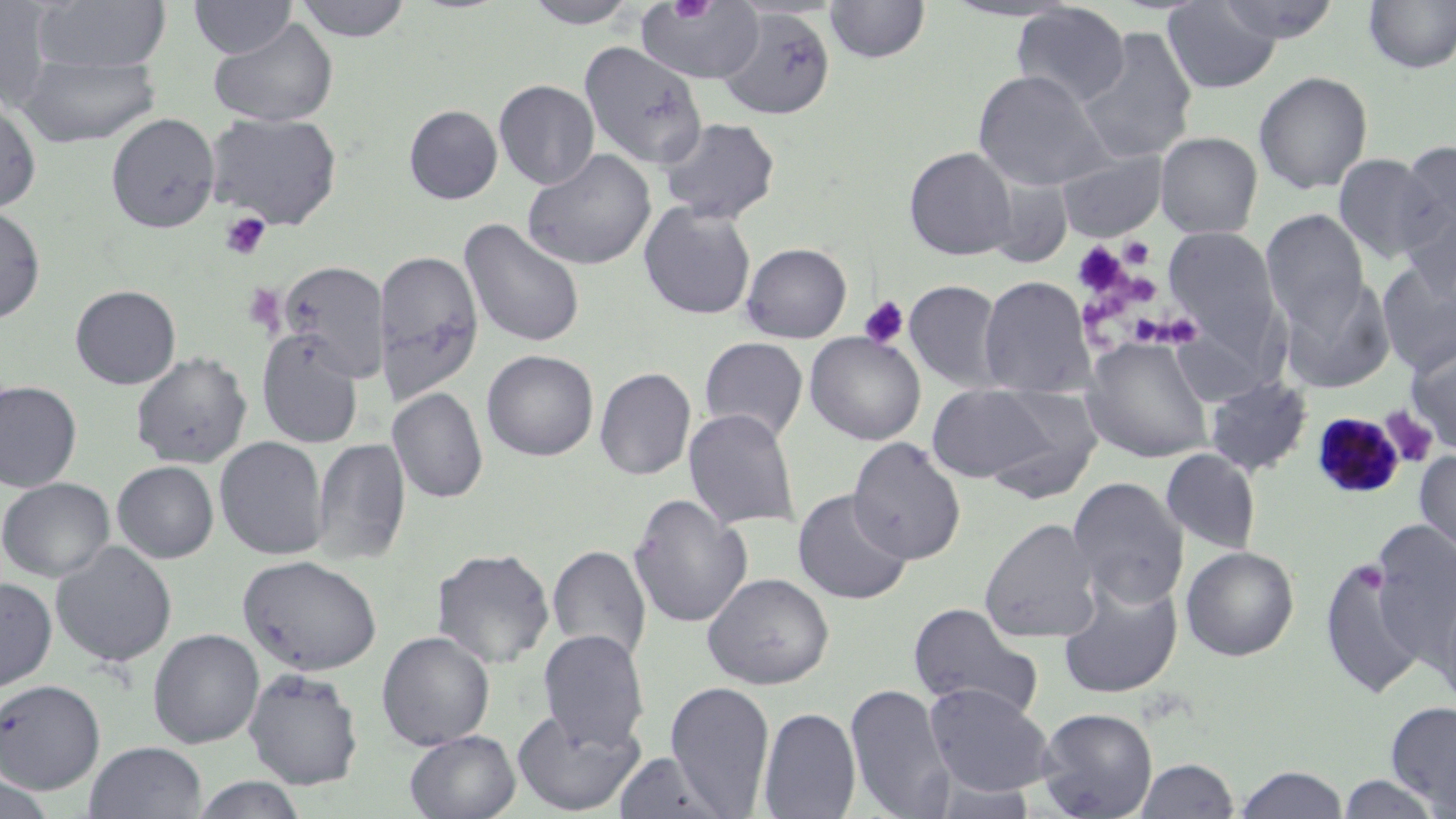
slide-level diagnosis = Plasmodium malariae
preparation = thin blood film
uninfected red blood cell locations = approximate bounding boxes as (x1, y1, x2, y2) in pixels: (0, 0, 57, 112), (31, 0, 172, 74), (293, 0, 413, 43), (521, 0, 642, 28), (824, 0, 930, 64), (939, 0, 1085, 23), (1213, 0, 1342, 43), (1362, 0, 1456, 75), (188, 1, 298, 59), (636, 1, 765, 86), (1162, 1, 1283, 93), (1011, 3, 1130, 109), (717, 7, 835, 121), (208, 17, 339, 127), (1077, 27, 1198, 163), (579, 40, 708, 169), (16, 55, 161, 147), (972, 69, 1111, 191), (1254, 70, 1374, 195), (494, 80, 600, 191), (0, 94, 42, 213), (404, 105, 502, 204), (205, 111, 343, 230), (106, 113, 220, 233), (658, 117, 780, 224), (1155, 131, 1263, 238), (1396, 141, 1455, 253), (904, 147, 1018, 260), (523, 148, 656, 271), (1055, 149, 1168, 241), (1333, 153, 1442, 265), (639, 201, 757, 320), (1399, 204, 1456, 305), (0, 205, 45, 325), (1261, 209, 1371, 335), (460, 218, 586, 349), (1164, 226, 1282, 359), (741, 242, 852, 343), (373, 249, 483, 402), (1376, 259, 1456, 376), (278, 261, 390, 380), (979, 276, 1093, 398), (1279, 276, 1395, 394), (903, 280, 1006, 392), (70, 285, 181, 389), (1167, 326, 1276, 405), (257, 331, 365, 448), (805, 332, 926, 445), (698, 337, 809, 443), (1081, 337, 1215, 463), (1405, 338, 1456, 453), (482, 350, 599, 461), (131, 351, 252, 468), (594, 367, 696, 481), (1204, 375, 1312, 477), (0, 380, 82, 492), (925, 382, 1073, 486), (389, 387, 488, 504), (683, 408, 800, 531), (215, 436, 329, 560), (311, 437, 410, 566), (847, 437, 966, 565), (1161, 448, 1261, 554), (1414, 448, 1456, 569), (112, 461, 219, 563), (1067, 476, 1188, 609), (1, 477, 115, 582), (792, 489, 913, 605), (629, 493, 751, 629), (979, 517, 1102, 643), (1368, 519, 1456, 678), (50, 541, 178, 668), (548, 544, 651, 667), (1181, 545, 1299, 661), (431, 547, 555, 669), (1319, 549, 1430, 700), (237, 554, 382, 676), (702, 573, 834, 690), (0, 576, 58, 693), (1057, 578, 1183, 700), (1432, 579, 1456, 716), (908, 602, 1044, 720), (148, 628, 264, 749), (538, 629, 649, 752), (376, 631, 495, 750), (243, 668, 363, 789), (0, 679, 105, 794), (665, 681, 776, 816), (925, 682, 1056, 796), (845, 683, 955, 818), (1386, 701, 1456, 815), (511, 705, 646, 815), (758, 706, 861, 819), (1037, 707, 1158, 818), (405, 730, 520, 819), (83, 741, 208, 818), (613, 751, 733, 819), (1136, 757, 1239, 818), (1234, 765, 1349, 818), (0, 772, 58, 818), (1335, 774, 1446, 818), (189, 775, 310, 819)
field of view = single
modality = optical microscopy
platelet locations = approximate bounding boxes as (x1, y1, x2, y2) in pixels: (667, 0, 717, 24), (218, 212, 271, 261), (1118, 236, 1156, 270), (1073, 241, 1131, 298), (1124, 273, 1161, 306), (242, 283, 286, 333), (857, 295, 910, 349), (1082, 298, 1130, 328), (1135, 310, 1197, 346), (1127, 313, 1167, 345), (1377, 404, 1440, 469)
image size = 1456×819 pixels
magnification = 1000x
Plasmodium malariae-infected red blood cell locations = approximate bounding boxes as (x1, y1, x2, y2) in pixels: (1312, 411, 1407, 501)
stain = May-Grünwald-Giemsa